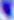

modality = micrograph
identification = Toxoplasma gondii
magnification = 400x